Report the malaria status of this cell.
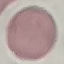
It is uninfected.

stain = Giemsa
preparation = thin smear
image type = automatically extracted cell patch, resized to 64 × 64 pixels
capture = smartphone through the microscope eyepiece